State which parasite is depicted.
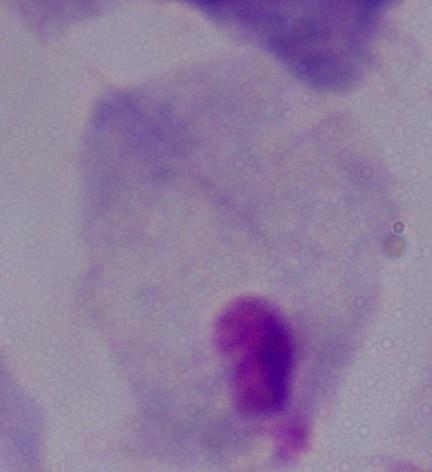
A trichomonad.

1000x magnification. Micrograph.